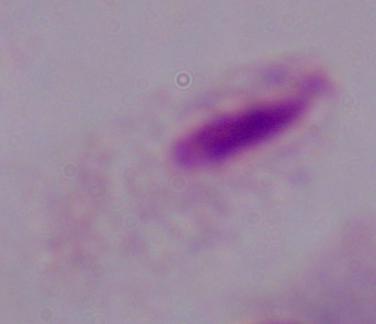
modality = micrograph
identification = trichomonad
magnification = 1000x